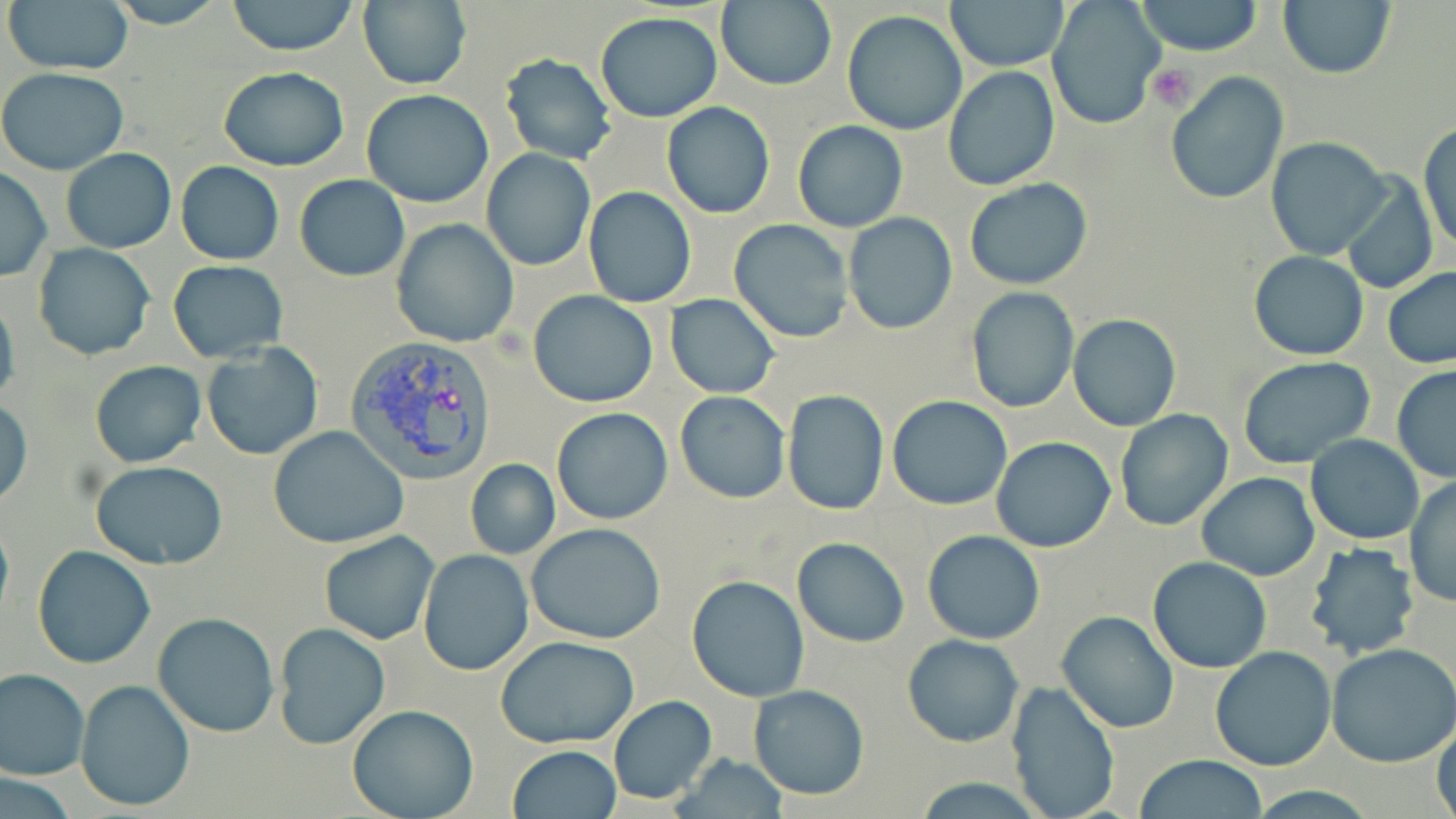

Summary:
  - Coordinate format: approximate bounding boxes as (x1,y1)-(x2,y2) corner pairs in pixels
  - Platelet locations: (1148,63)-(1196,112)
  - Uninfected red blood cell locations: (3,0)-(135,77), (102,0)-(229,28), (226,0)-(360,56), (716,0)-(836,93), (1047,0)-(1164,129), (1277,0)-(1397,81), (946,1)-(1068,72), (1137,1)-(1262,56), (357,2)-(472,89), (841,10)-(968,136), (594,11)-(723,122), (499,54)-(616,165), (218,66)-(348,170), (942,66)-(1061,191), (0,68)-(128,174), (1166,72)-(1290,207), (361,88)-(494,208), (662,102)-(775,218), (1419,120)-(1455,256), (792,121)-(908,232), (1267,137)-(1391,260), (61,147)-(176,254), (480,148)-(597,272), (175,162)-(284,264), (0,166)-(51,283), (294,174)-(410,282), (1340,174)-(1437,295), (964,177)-(1093,290), (583,186)-(697,309), (843,213)-(957,333), (391,219)-(519,349), (729,219)-(855,341), (32,242)-(155,361), (1248,250)-(1368,360), (169,260)-(288,363), (1383,267)-(1456,370), (965,287)-(1079,412), (528,290)-(658,408), (0,292)-(19,413), (664,293)-(781,399), (1067,314)-(1181,431), (202,343)-(323,460), (1238,356)-(1374,469), (91,359)-(205,468), (1391,364)-(1456,484), (782,389)-(888,514), (674,390)-(791,504), (887,395)-(1013,510), (0,400)-(32,509), (551,407)-(674,526), (1114,409)-(1232,531), (268,426)-(408,550), (1306,435)-(1425,544), (990,437)-(1116,553), (465,458)-(560,560), (90,461)-(229,570), (1197,473)-(1320,581), (1405,474)-(1456,608), (0,513)-(13,630), (526,524)-(667,645), (921,530)-(1046,645), (319,531)-(439,645), (793,537)-(909,648), (1304,542)-(1418,658), (33,546)-(156,669), (418,549)-(534,676), (1147,557)-(1272,674), (686,574)-(811,703), (1057,610)-(1180,734), (151,612)-(278,737), (273,621)-(391,749), (902,634)-(1024,747), (496,637)-(640,749), (1327,644)-(1456,768), (1209,646)-(1336,772), (0,668)-(90,780), (75,679)-(195,812), (1005,679)-(1121,819), (749,685)-(870,799), (608,695)-(716,805), (347,703)-(478,819), (1432,719)-(1456,819), (505,745)-(622,819), (673,756)-(791,818), (1132,756)-(1271,819), (0,771)-(77,817)
  - Plasmodium vivax-infected red blood cell locations: (346,336)-(499,484)
  - Slide-level diagnosis: Plasmodium vivax
  - Modality: light microscopy
  - Magnification: 1000x
  - Preparation: thin blood film
  - Image size: 1456×819 pixels
  - Field of view: single
  - Stain: May-Grünwald-Giemsa